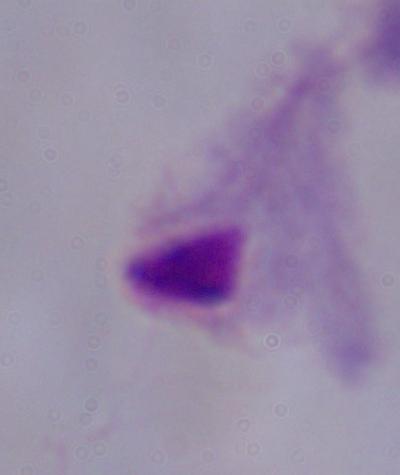
identification = trichomonad
magnification = 1000x
modality = photomicrograph